Locate every Plasmodium parasite.
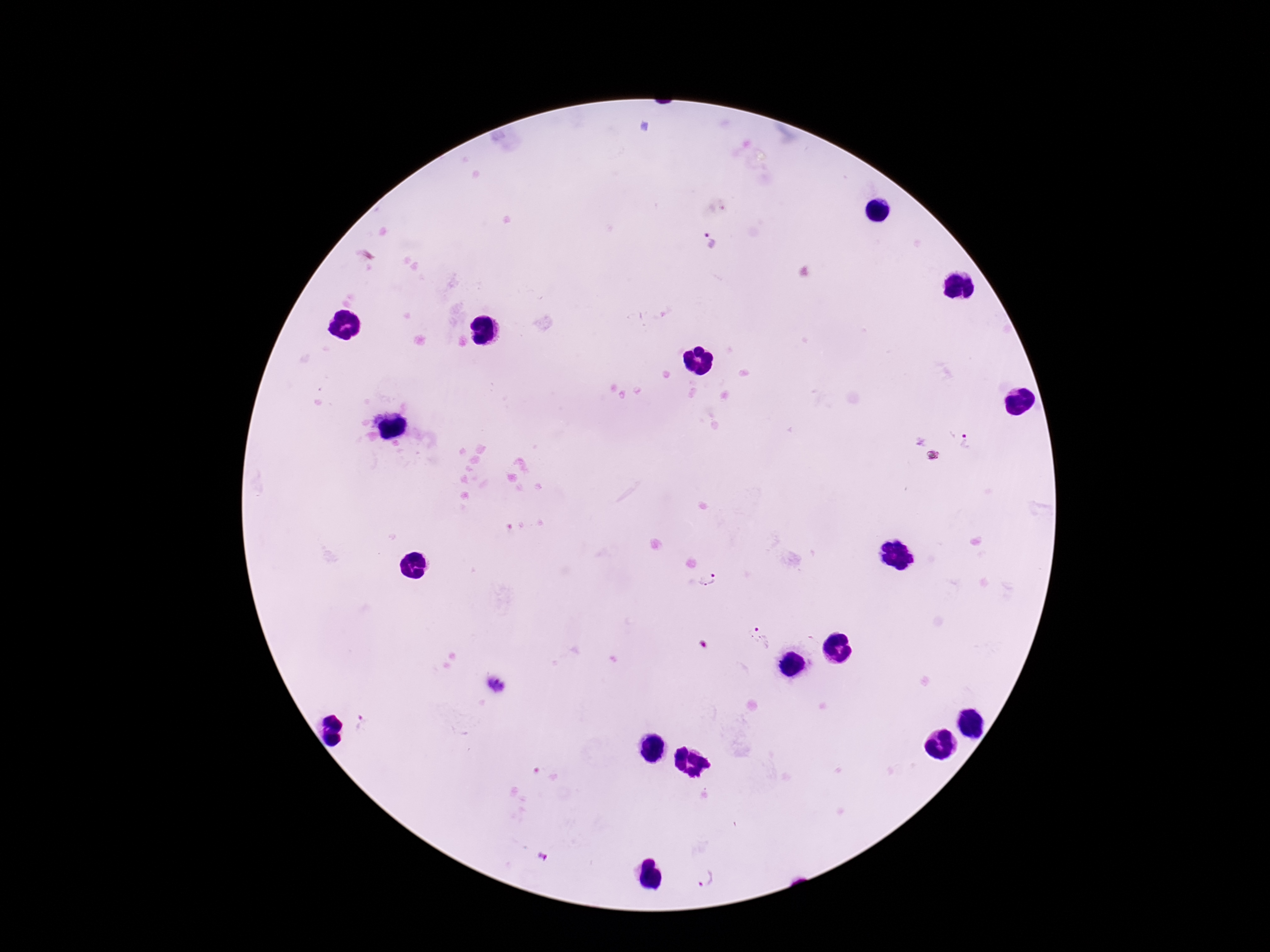

Approximate object centers, in pixels from the top-left corner.
Plasmodium parasites: (x=710, y=242), (x=967, y=442), (x=709, y=582), (x=761, y=637), (x=496, y=686), (x=363, y=725), (x=546, y=774), (x=543, y=859), (x=705, y=879).

Summary:
  - Capture: smartphone camera through the microscope eyepiece
  - Image size: 1270×952 pixels
  - Preparation: thick peripheral-blood smear
  - Magnification: 100x
  - Field of view: single
  - Patient malaria status: positive
  - Stain: Giemsa